Classify this cell by malaria status.
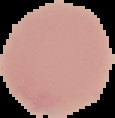

Uninfected.

Summary:
  - Image size: 115×118 pixels
  - Preparation: thin blood film
  - Image type: segmented cell region on a black background